Report the malaria status of this cell.
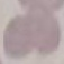

It is uninfected.

preparation = thin blood smear
capture = smartphone camera at the microscope eyepiece
stain = Giemsa
image type = automatically extracted cell patch, resized to 64 × 64 pixels